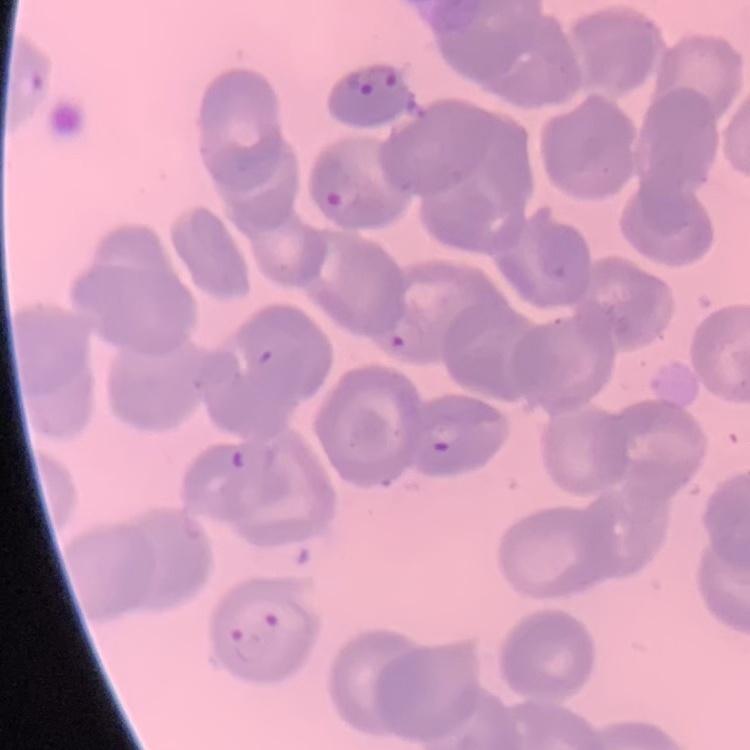
{
  "erythrocyte_morphology": "no rouleaux formation",
  "preparation": "thin peripheral smear",
  "image_type": "square crop of a larger photomicrograph",
  "stain": "Field's or Giemsa"
}